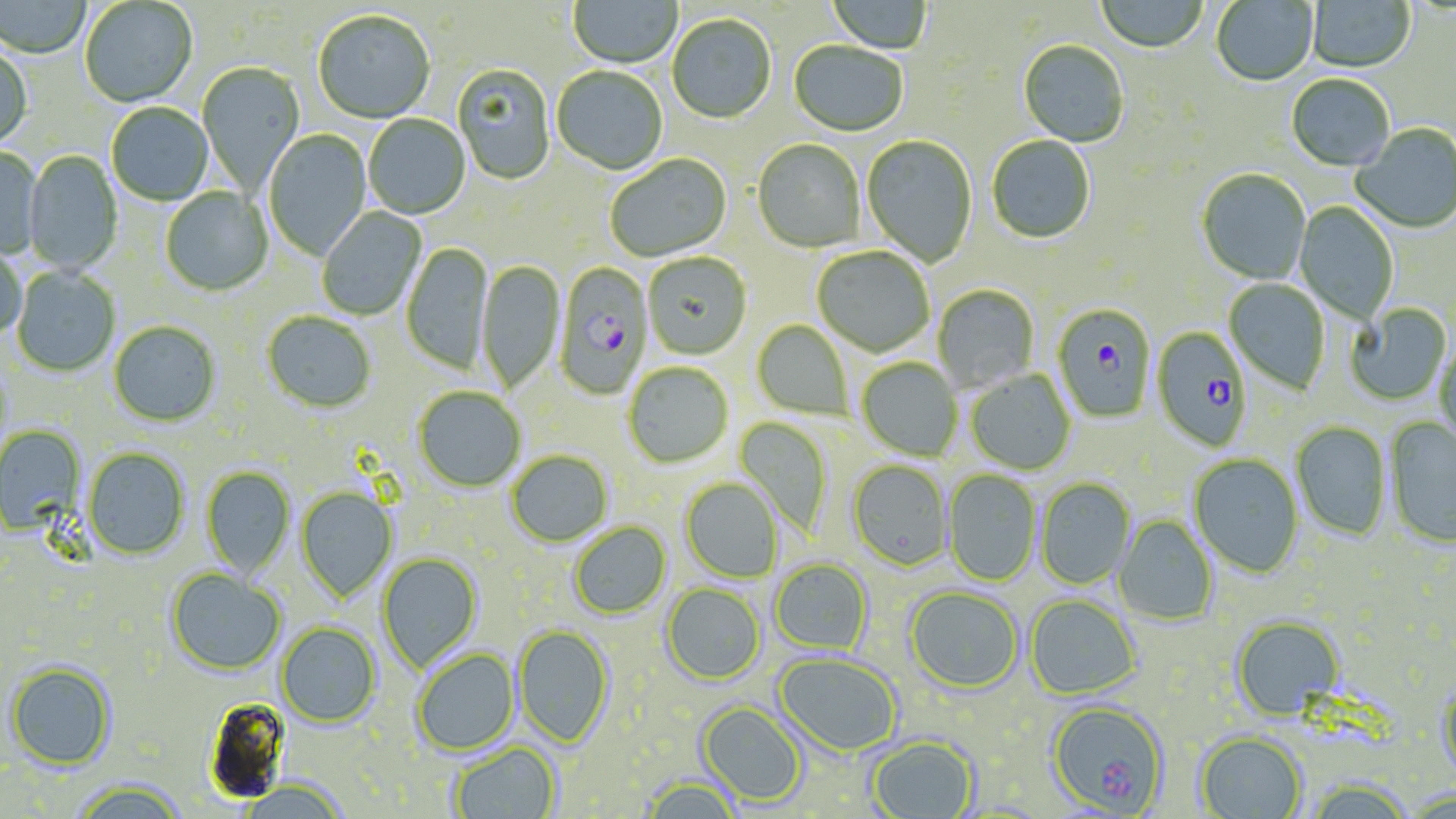

Approximate bounding boxes as (x1, y1, x2, y2) in pixels. Plasmodium falciparum-infected red blood cell locations: (555, 263, 653, 401), (1052, 305, 1157, 424), (1151, 327, 1251, 452). Uninfected red blood cell locations: (0, 0, 92, 59), (569, 0, 682, 71), (826, 0, 932, 55), (1095, 0, 1208, 55), (1211, 0, 1319, 87), (80, 1, 198, 109), (1307, 1, 1415, 74), (313, 12, 435, 125), (667, 16, 776, 126), (789, 41, 907, 138), (1018, 41, 1129, 148), (0, 45, 33, 152), (197, 62, 305, 194), (452, 65, 555, 186), (551, 67, 667, 176), (1286, 75, 1394, 173), (106, 103, 213, 206), (363, 114, 470, 220), (1350, 124, 1456, 234), (264, 129, 373, 261), (861, 135, 978, 267), (987, 136, 1096, 245), (752, 140, 865, 253), (0, 147, 44, 260), (23, 151, 123, 276), (605, 155, 731, 263), (1197, 169, 1311, 286), (160, 188, 273, 297), (1294, 201, 1399, 324), (317, 207, 427, 320), (401, 242, 494, 376), (0, 244, 26, 341), (811, 247, 935, 359), (643, 253, 752, 361), (477, 259, 565, 395), (12, 267, 120, 378), (1224, 278, 1330, 395), (932, 285, 1039, 392), (1344, 303, 1452, 406), (262, 313, 376, 415), (752, 320, 852, 421), (108, 322, 221, 428), (1434, 339, 1456, 455), (856, 357, 963, 461), (623, 362, 734, 470), (966, 369, 1076, 476), (414, 388, 526, 493), (734, 416, 833, 538), (1385, 417, 1456, 550), (1291, 422, 1391, 541), (0, 425, 86, 536), (83, 447, 190, 561), (506, 451, 612, 548), (1188, 454, 1304, 578), (847, 460, 952, 572), (201, 466, 295, 579), (943, 469, 1041, 586), (680, 478, 783, 584), (1036, 478, 1136, 589), (296, 487, 398, 603), (1114, 515, 1218, 626), (569, 522, 671, 620), (378, 554, 483, 672), (770, 559, 874, 656), (166, 570, 285, 677), (661, 583, 765, 686), (905, 587, 1023, 694), (1025, 595, 1141, 700), (1231, 616, 1345, 721), (276, 622, 381, 728), (513, 625, 614, 749), (412, 649, 519, 756), (774, 653, 902, 757), (6, 661, 116, 771), (1437, 680, 1456, 788), (204, 696, 293, 803), (1047, 701, 1169, 815), (697, 702, 808, 807), (1195, 732, 1307, 819), (868, 736, 979, 819), (450, 742, 562, 819), (642, 777, 741, 819), (68, 781, 189, 819), (238, 781, 351, 819), (1304, 781, 1416, 819). Slide-level diagnosis: Plasmodium falciparum. Image is 1456×819 pixels. Thin blood film. One field of a larger specimen. Optical microscopy. 1000x magnification. May-Grünwald-Giemsa-stained preparation.